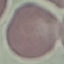
Malaria status: uninfected. Acquired by smartphone through the microscope eyepiece. Thin blood smear. Automatically extracted cell patch, resized to 64 × 64 pixels. Giemsa-stained preparation.